Assess for Plasmodium parasites.
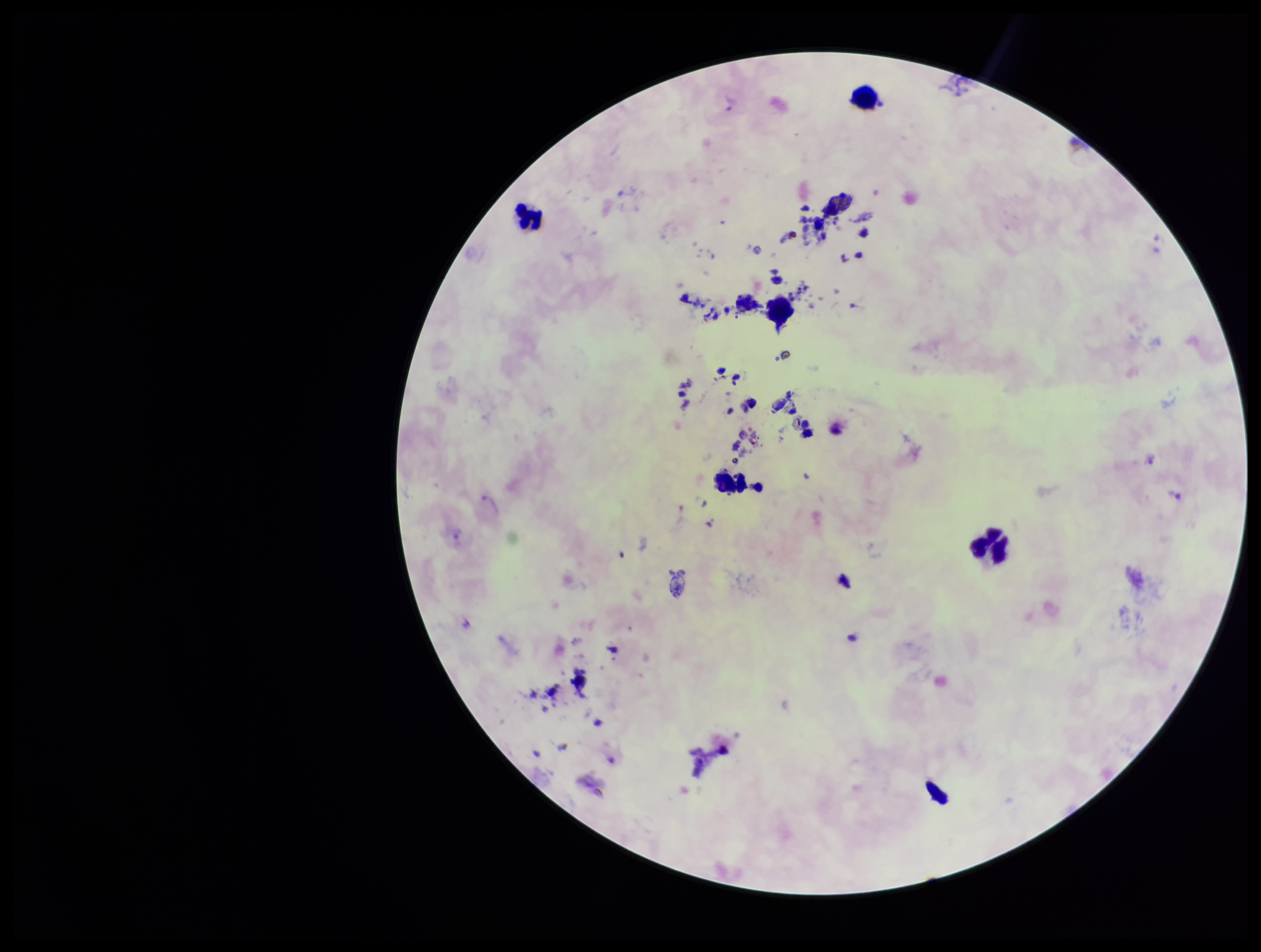
Detected.

Summary:
  - Stain: Giemsa
  - Leukocyte count: 5
  - Patient malaria status: infected
  - Preparation: thick blood smear
  - Field of view: single
  - Parasite count: 8
  - Image size: 1261×952 pixels
  - Capture: smartphone photograph through the microscope eyepiece
  - Species reported for this patient: Plasmodium vivax